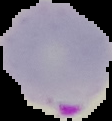

Cell region segmented out of the field of view; the surrounding area is masked to black. Result: malaria parasites identified. From a thin blood smear. Image is 112×121 pixels.